Identify the parasite.
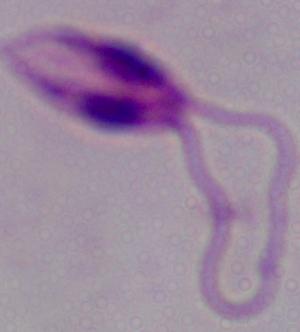

Leishmania.

Summary:
  - Modality: photomicrograph
  - Magnification: 1000x